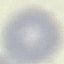

{
  "result": "no malaria parasites detected",
  "image_type": "automatically extracted cell patch, resized to 64 × 64 pixels",
  "capture": "smartphone camera at the microscope eyepiece",
  "preparation": "thin smear",
  "stain": "Giemsa"
}